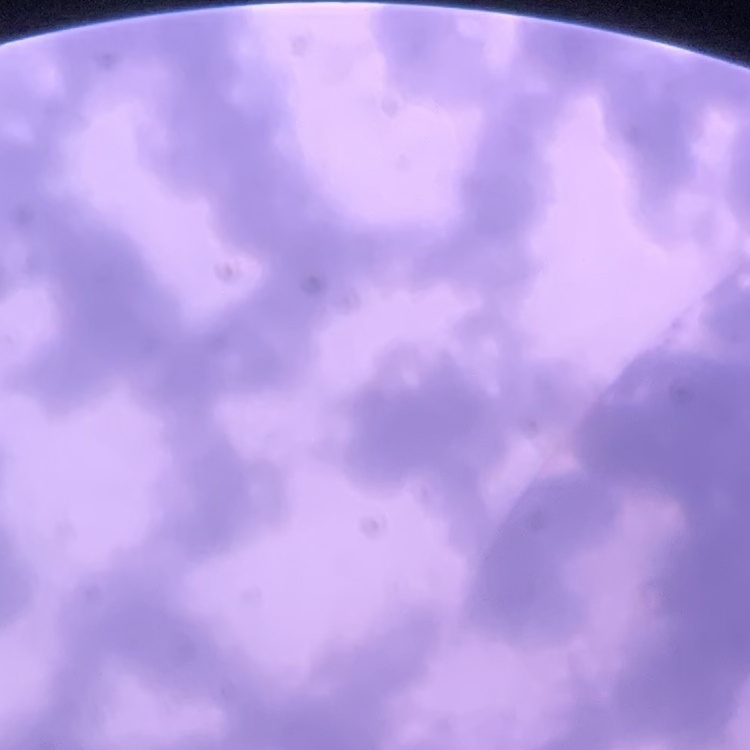
erythrocyte morphology = rouleaux formation
stain = Field's or Giemsa
preparation = thin blood smear
image type = square crop of a larger photomicrograph